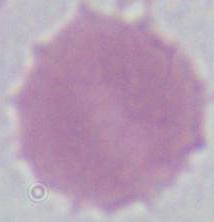
{
  "identification": "red blood cell",
  "modality": "micrograph",
  "magnification": "1000x"
}